Classify this cell by malaria status.
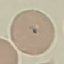
Uninfected.

Summary:
  - Image type: cell patch, automatically extracted from a larger field of view and resized to 64 × 64 pixels
  - Preparation: thin blood smear
  - Capture: smartphone camera at the microscope eyepiece
  - Stain: Giemsa